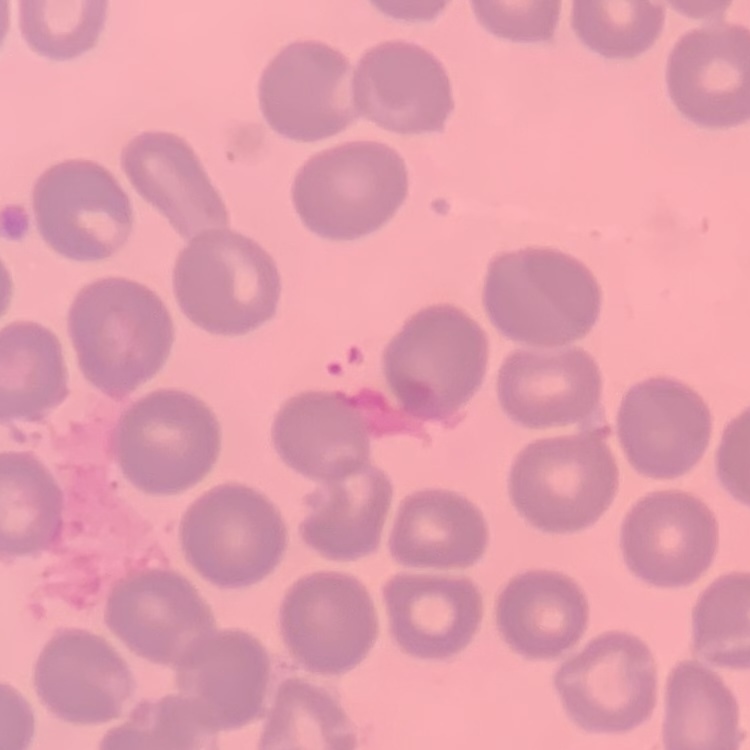
erythrocyte_morphology: no rouleaux formation
preparation: thin blood film
image_type: square crop of a larger photomicrograph
stain: Field's or Giemsa